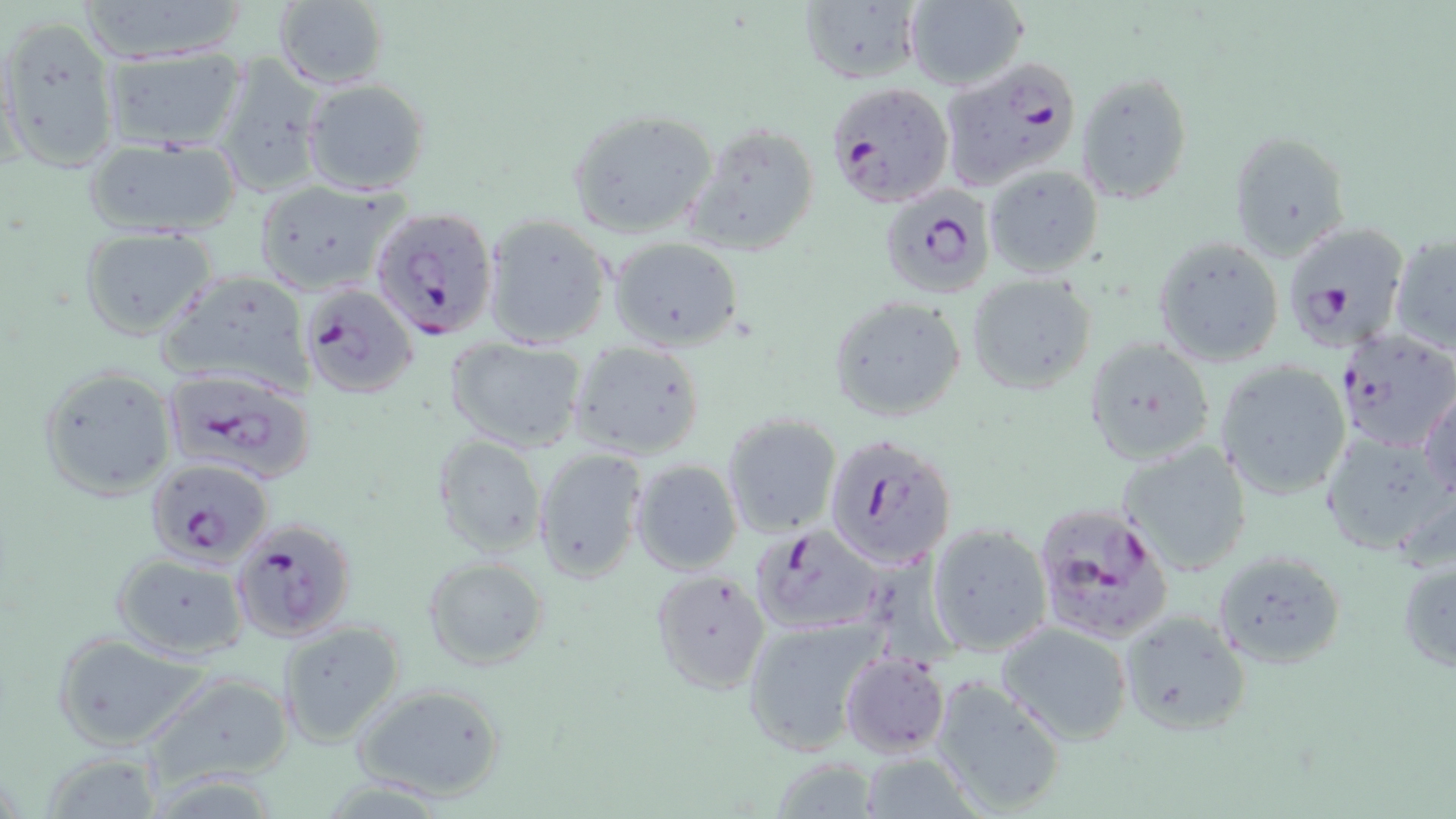
Summary:
  - Coordinate format: approximate bounding boxes as (x1,y1)-(x2,y2) corner pairs in pixels
  - Plasmodium falciparum-infected red blood cell locations: (944,57)-(1080,190), (824,81)-(954,208), (876,186)-(994,300), (370,206)-(498,342), (1282,220)-(1412,352), (300,284)-(419,399), (1334,327)-(1455,452), (39,365)-(178,501), (162,370)-(316,484), (824,434)-(956,569), (145,457)-(272,565), (1031,503)-(1174,645), (230,517)-(357,642), (749,524)-(887,637)
  - Uninfected red blood cell locations: (77,0)-(256,60), (273,1)-(388,91), (904,1)-(1029,91), (797,2)-(923,86), (0,16)-(121,172), (99,46)-(246,152), (211,53)-(329,198), (1077,71)-(1194,202), (303,79)-(429,195), (565,108)-(718,239), (681,120)-(821,260), (1229,130)-(1349,261), (81,135)-(244,239), (984,164)-(1105,278), (253,180)-(408,295), (483,215)-(613,349), (79,226)-(217,341), (1389,230)-(1456,356), (1152,235)-(1286,368), (608,238)-(744,350), (157,271)-(313,394), (966,274)-(1097,393), (827,297)-(967,422), (1085,337)-(1215,467), (443,338)-(590,454), (569,340)-(705,460), (1215,360)-(1354,500), (1417,389)-(1455,504), (721,413)-(844,539), (1320,430)-(1451,556), (432,435)-(548,560), (1118,439)-(1253,577), (533,447)-(646,582), (630,459)-(743,575), (925,522)-(1053,657), (1212,548)-(1346,669), (1396,549)-(1456,673), (111,551)-(251,660), (423,557)-(550,670), (650,569)-(771,693), (1117,609)-(1250,737), (740,614)-(886,756), (277,619)-(406,747), (993,621)-(1135,746), (52,635)-(212,749), (839,651)-(950,757), (136,671)-(296,788), (930,676)-(1069,815), (353,683)-(507,802), (860,750)-(980,819), (36,752)-(164,817), (763,757)-(880,817)
  - Slide-level diagnosis: Plasmodium falciparum
  - Magnification: 1000x
  - Modality: optical microscopy
  - Field of view: single
  - Stain: May-Grünwald-Giemsa
  - Image size: 1456×819 pixels
  - Preparation: thin blood smear